Name the blood parasite species.
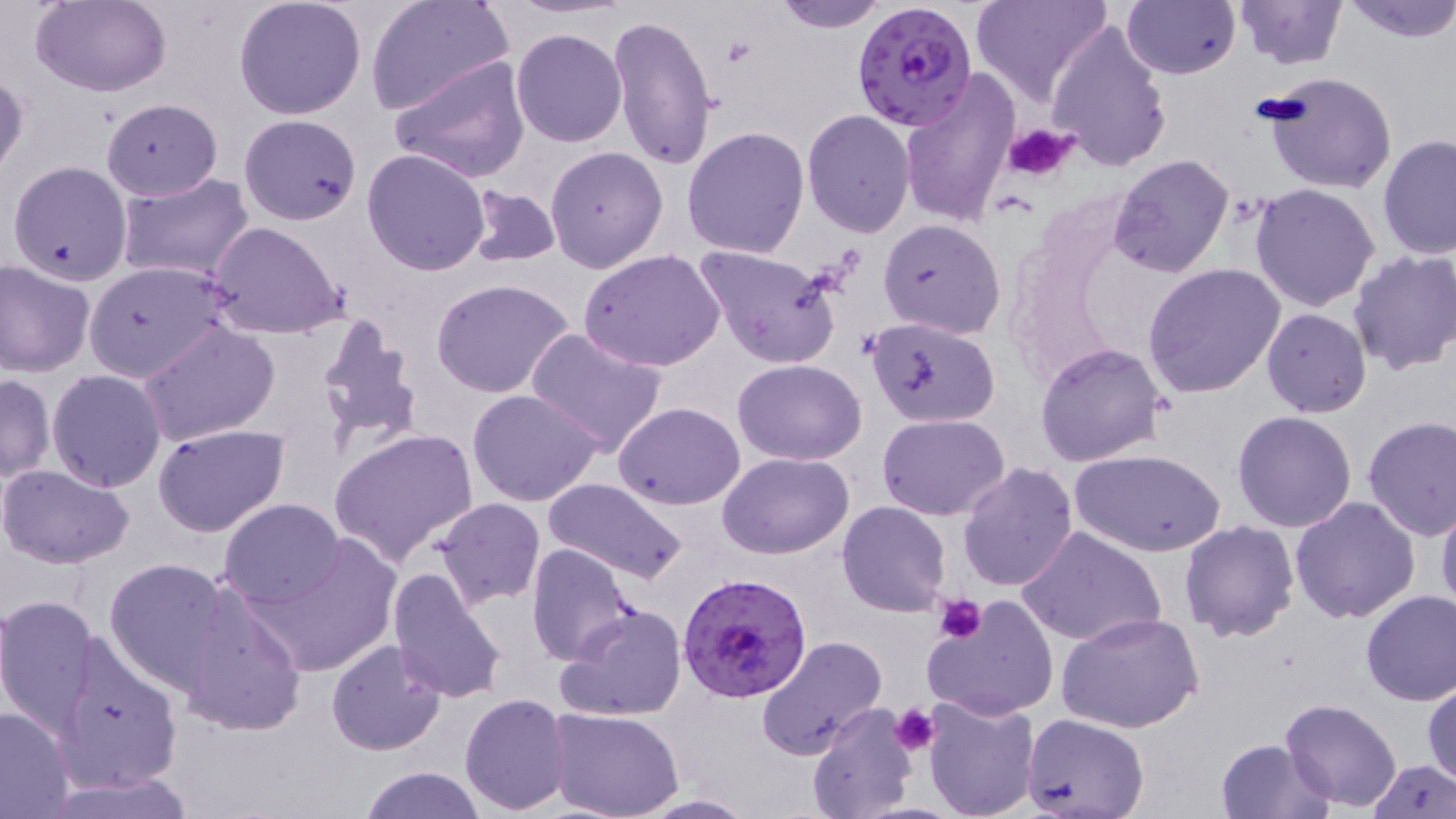

Plasmodium falciparum.

Summary:
  - Coordinate format: approximate bounding boxes as (x1, y1, x2, y2) in pixels
  - Platelet locations: (1007, 123, 1077, 182), (934, 595, 987, 644), (890, 704, 940, 757)
  - Plasmodium falciparum-infected red blood cell locations: (851, 2, 978, 134), (679, 572, 812, 702)
  - Uninfected red blood cell locations: (30, 0, 172, 97), (233, 0, 367, 119), (365, 0, 513, 119), (770, 0, 893, 29), (971, 0, 1112, 109), (1121, 0, 1239, 79), (1230, 0, 1347, 70), (1338, 0, 1456, 42), (609, 12, 718, 171), (1044, 16, 1172, 171), (511, 28, 627, 147), (391, 55, 530, 184), (1, 67, 28, 181), (1260, 70, 1397, 194), (898, 71, 1018, 228), (101, 99, 222, 200), (802, 110, 916, 237), (238, 114, 363, 226), (683, 126, 809, 257), (1378, 134, 1456, 263), (544, 147, 667, 273), (362, 149, 491, 276), (1108, 154, 1236, 278), (6, 160, 133, 285), (115, 171, 253, 283), (1250, 184, 1381, 314), (464, 186, 560, 267), (877, 218, 1007, 338), (206, 220, 349, 341), (692, 244, 840, 368), (1348, 249, 1456, 375), (579, 250, 727, 372), (0, 259, 95, 376), (85, 261, 226, 383), (1144, 262, 1285, 398), (431, 278, 575, 398), (1261, 307, 1372, 418), (312, 313, 422, 453), (867, 316, 1002, 427), (138, 320, 280, 446), (525, 327, 669, 458), (1035, 343, 1168, 466), (733, 358, 868, 465), (47, 370, 167, 492), (1, 373, 55, 482), (466, 388, 605, 507), (613, 402, 745, 509), (1233, 410, 1359, 532), (877, 412, 1010, 521), (1363, 416, 1456, 540), (152, 423, 290, 538), (328, 428, 480, 567), (1074, 449, 1224, 558), (719, 451, 855, 559), (955, 462, 1078, 593), (0, 464, 135, 567), (542, 478, 689, 587), (1436, 494, 1456, 619), (1289, 496, 1421, 625), (219, 498, 345, 606), (431, 498, 547, 608), (837, 501, 951, 616), (1179, 520, 1300, 642), (1016, 525, 1167, 648), (239, 534, 403, 680), (524, 544, 638, 666), (103, 558, 232, 693), (387, 566, 509, 704), (179, 585, 309, 739), (1359, 589, 1456, 706), (0, 595, 102, 735), (923, 597, 1059, 722), (555, 602, 686, 722), (1058, 611, 1204, 734), (53, 631, 183, 793), (757, 635, 888, 759), (324, 639, 447, 757), (1422, 680, 1456, 789), (460, 692, 572, 812), (920, 695, 1041, 819), (1280, 697, 1403, 809), (807, 702, 918, 819), (0, 706, 76, 818), (548, 708, 684, 819), (1021, 714, 1149, 817), (1215, 738, 1333, 818), (1368, 758, 1455, 818), (357, 765, 486, 819), (45, 772, 199, 819), (633, 793, 758, 818)
  - Preparation: thin blood film
  - Stain: May-Grünwald-Giemsa
  - Modality: light microscopy
  - Field of view: one of a larger specimen
  - Magnification: 1000x
  - Image size: 1456×819 pixels